State the preparation type.
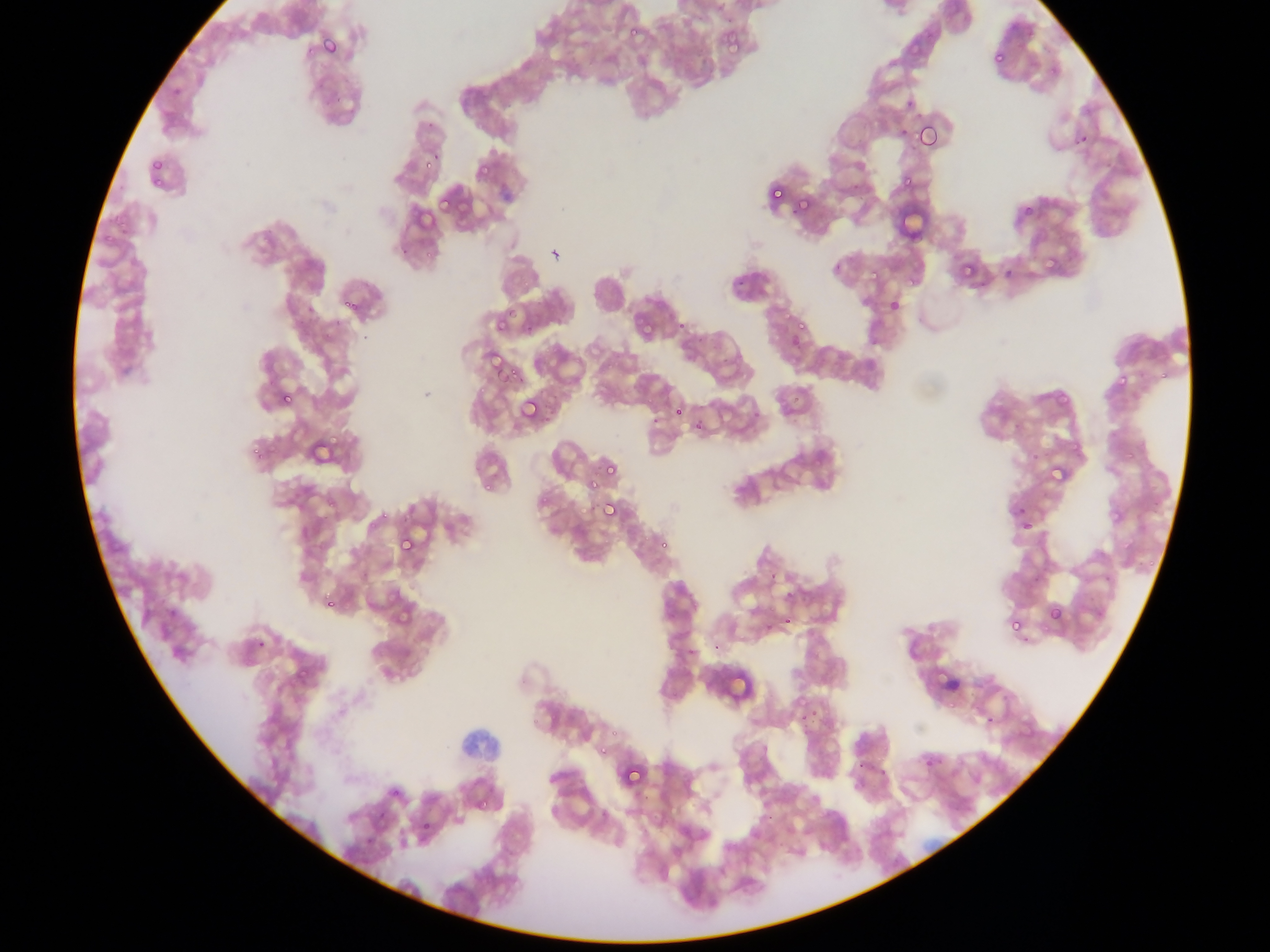
Thin blood smear.

country = Ghana
field of view = single
capture = mobile-phone photograph through a microscope
malaria parasite locations = approximate bounding boxes as left top right bottom in pixels: 621 22 637 40; 718 27 747 55; 317 32 345 62; 987 43 1006 64; 992 51 1005 65; 915 121 942 152; 423 161 431 171; 482 163 490 175; 898 172 917 189; 769 186 786 206; 436 188 459 213; 799 200 811 215; 1023 206 1034 217; 958 258 984 277; 902 271 918 285; 867 272 879 287; 342 295 364 318; 886 297 903 316; 777 307 791 324; 492 316 508 332; 794 317 811 333; 642 322 657 339; 491 357 518 386; 1111 374 1128 390; 277 391 293 408; 1054 393 1073 410; 518 395 543 423; 670 402 698 428; 672 405 686 420; 690 415 708 434; 327 435 342 447; 1068 436 1080 449; 1124 444 1136 460; 311 445 323 462; 602 451 621 478; 1047 462 1070 486; 585 477 601 494; 599 498 621 522; 1013 503 1031 525; 1107 504 1122 521; 1016 515 1035 534; 395 532 417 558; 656 537 669 553; 322 597 338 613; 394 602 411 624; 1046 603 1066 625; 164 605 180 621; 779 612 796 629; 1006 616 1023 636; 760 620 780 640; 297 666 316 682; 600 742 611 757; 921 754 938 772; 619 761 645 789; 475 795 494 812
image size = 1270×952 pixels